Assess this cell for malaria.
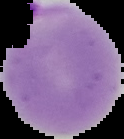
Parasitized.

preparation: thin blood film
image_type: segmented cell region on a black background
image_size: 124×139 pixels